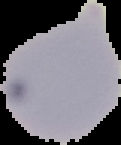

Summary:
  - Preparation: thin blood smear
  - Result: negative for Plasmodium parasites
  - Image size: 121×145 pixels
  - Image type: cell region segmented out of the field of view; surrounding area masked to black